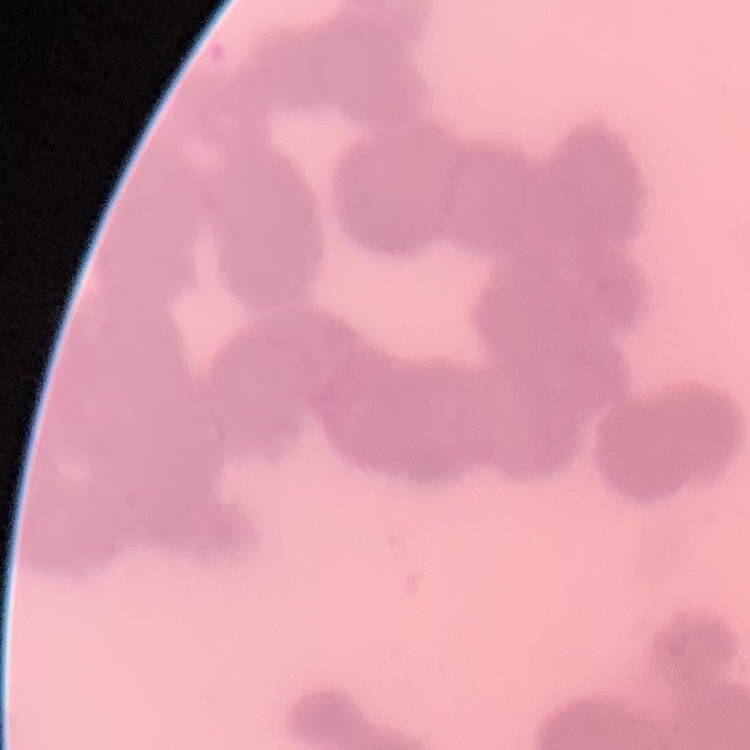

red blood cell morphology = rouleaux formation
image type = one tile cut from a larger photomicrograph
stain = Field's or Giemsa
preparation = thin blood film